Give the preparation type.
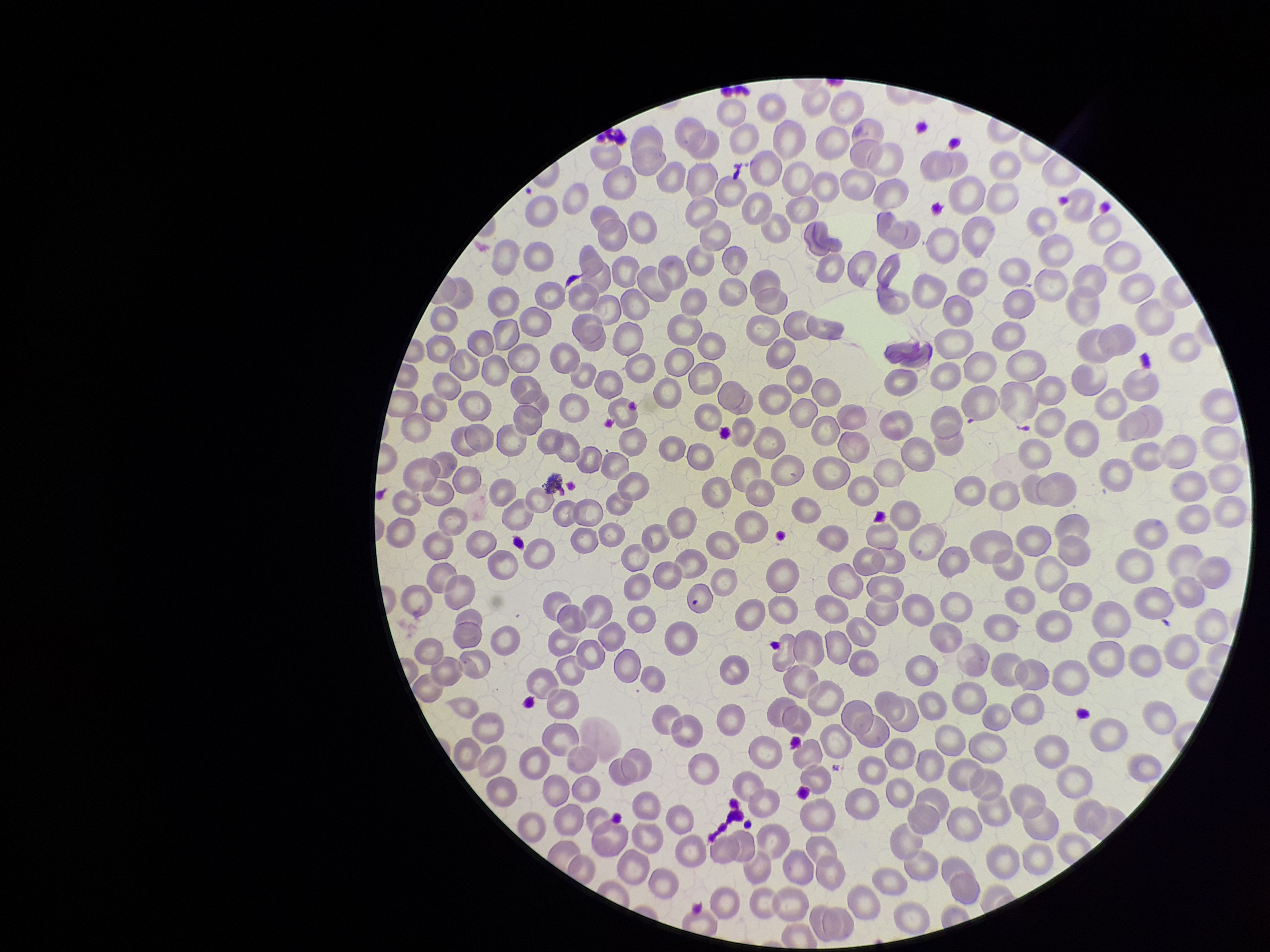

It is a thin blood smear.

Stained with Giemsa. Parasitized red blood cells: none seen. One field from this slide. Parasitized red blood cell count: 0. Red blood cell count: 269. Image is 1270×952 pixels. Patient malaria status: negative. Smartphone photograph taken through the eyepiece of a microscope.